Locate every Plasmodium falciparum-infected red blood cell.
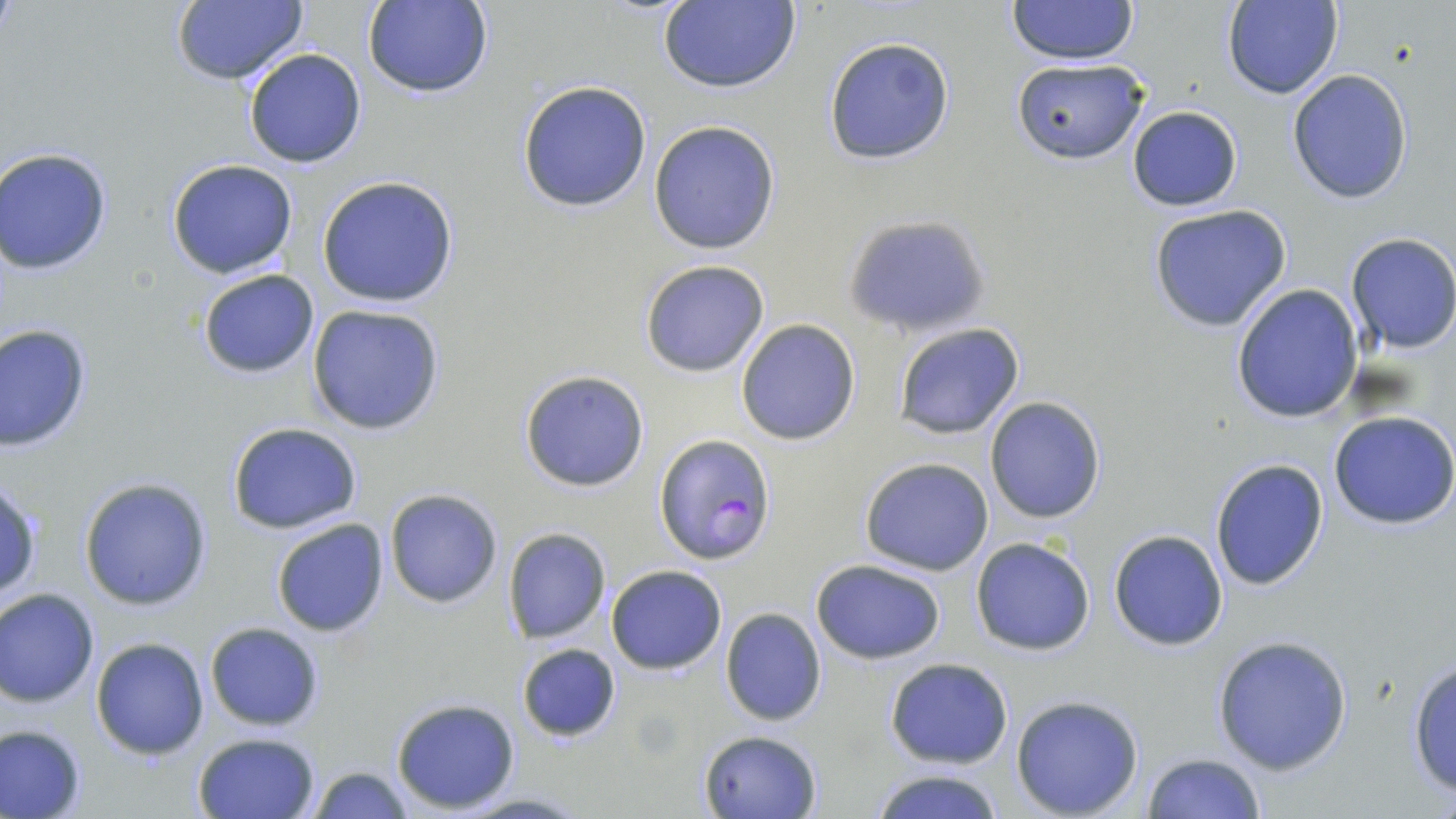

Approximate bounding boxes as [x1, y1, x2, y2] in pixels.
Plasmodium falciparum-infected red blood cells: [654, 433, 775, 565].

Uninfected red blood cell locations: [361, 0, 494, 99], [1006, 0, 1139, 65], [1223, 0, 1344, 100], [169, 1, 309, 86], [656, 1, 802, 94], [823, 36, 955, 165], [244, 48, 366, 168], [1009, 58, 1149, 164], [1285, 68, 1415, 205], [517, 81, 654, 213], [1126, 104, 1242, 211], [648, 120, 781, 254], [0, 147, 113, 276], [166, 160, 297, 280], [317, 175, 458, 308], [1147, 203, 1293, 332], [843, 212, 989, 340], [1345, 233, 1456, 355], [639, 259, 770, 377], [197, 268, 320, 378], [1230, 284, 1363, 424], [306, 303, 446, 434], [734, 318, 862, 446], [1, 323, 92, 451], [893, 323, 1027, 440], [518, 370, 650, 492], [984, 398, 1107, 522], [1329, 411, 1456, 528], [226, 421, 362, 534], [857, 456, 995, 575], [1209, 458, 1329, 592], [79, 478, 213, 610], [1, 479, 42, 603], [384, 489, 504, 608], [271, 519, 391, 638], [504, 527, 611, 643], [1108, 529, 1228, 651], [970, 536, 1097, 656], [810, 557, 946, 665], [606, 564, 727, 673], [0, 588, 101, 708], [719, 607, 828, 727], [203, 621, 325, 733], [1210, 635, 1355, 774], [91, 637, 211, 758], [515, 642, 621, 743], [884, 657, 1014, 769], [1405, 657, 1456, 800], [1010, 694, 1145, 818], [391, 697, 521, 813], [0, 723, 87, 818], [699, 730, 821, 818], [192, 731, 321, 819], [1140, 752, 1268, 819], [305, 764, 416, 819], [866, 767, 1009, 819]. Slide-level diagnosis: Plasmodium falciparum. May-Grünwald-Giemsa-stained preparation. Image is 1456×819 pixels. Captured at 1000x magnification. Single field of view. Optical microscopy. Thin blood smear.